Identify the preparation type.
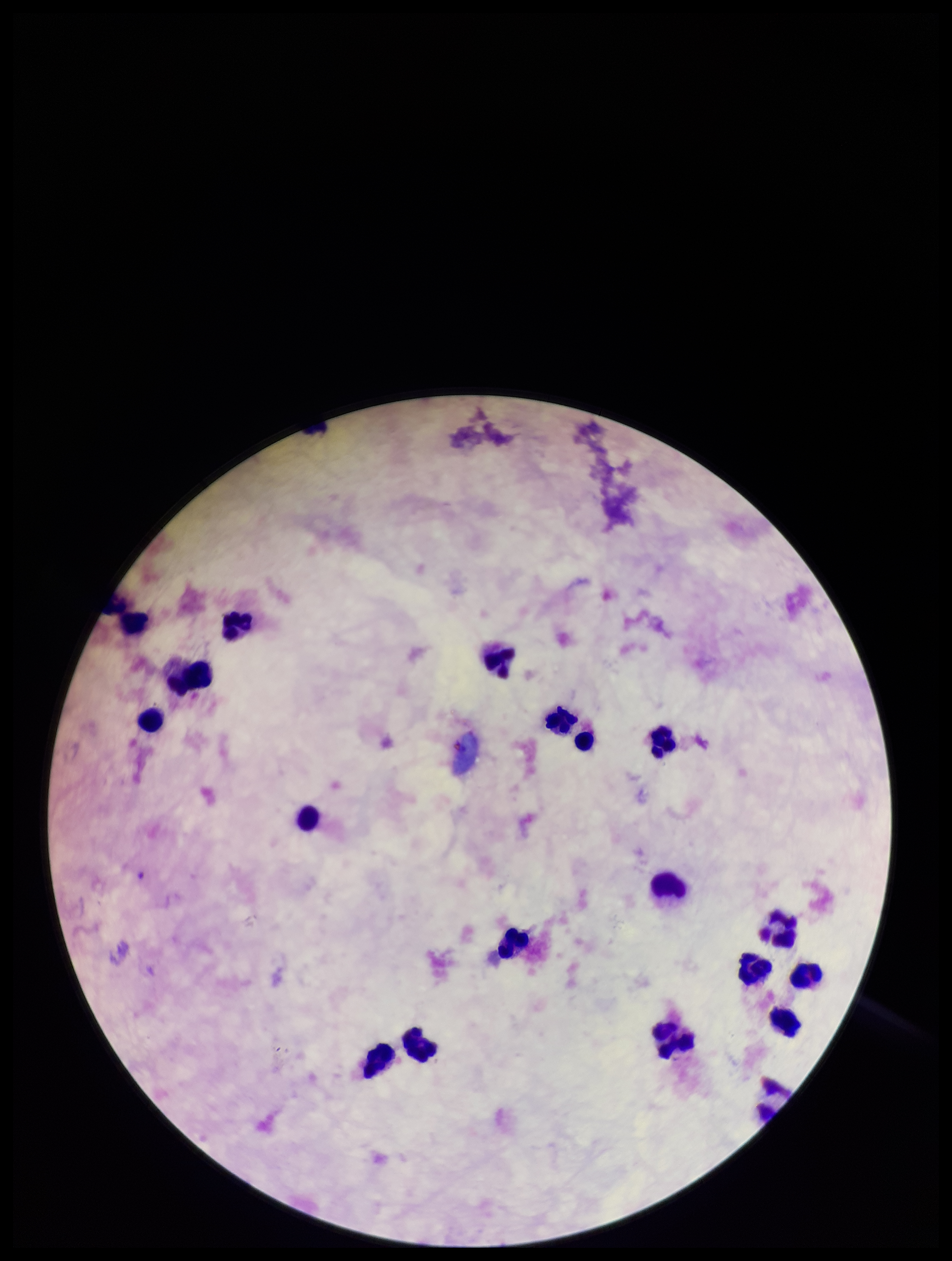

Thick.

Image is 952×1261 pixels. Plasmodium parasites: none detected. Smartphone photograph taken through the eyepiece of a microscope. Patient malaria status: negative. One field from this slide. Leukocyte count: 19. Stained with Giemsa. Parasite count: 0.